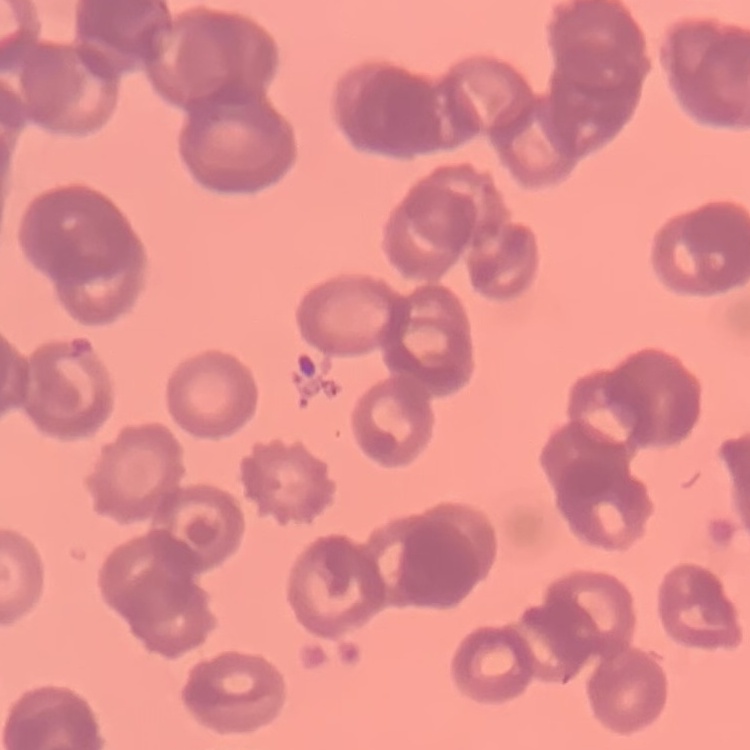

Summary:
  - Red blood cell morphology: rouleaux formation
  - Image type: square crop of a larger photomicrograph
  - Preparation: thin peripheral smear
  - Stain: Field's or Giemsa